Locate every blood parasite and identify its species.
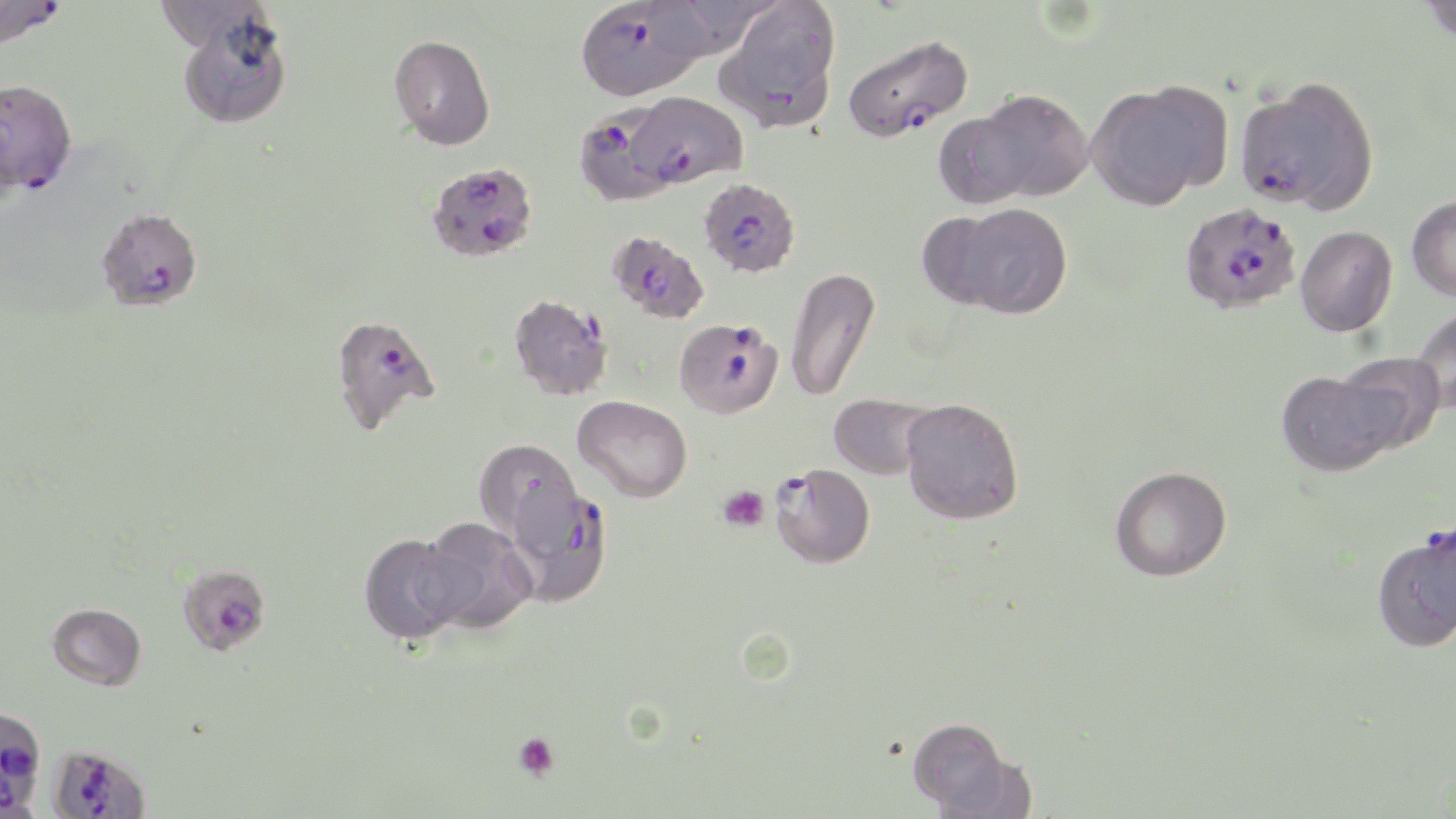
Approximate bounding boxes as (x1,y1)-(x2,y2) corner pairs in pixels.
Plasmodium falciparum-infected red blood cells: (0,0)-(67,50), (575,0)-(709,101), (841,33)-(973,143), (0,78)-(77,195), (1233,78)-(1378,213), (616,90)-(748,192), (579,105)-(690,208), (427,162)-(538,262), (699,177)-(801,278), (1179,202)-(1301,314), (95,207)-(203,312), (608,230)-(710,324), (507,293)-(614,401), (329,313)-(442,435), (674,317)-(784,419), (770,462)-(875,568), (504,482)-(614,607), (1406,530)-(1456,631), (176,563)-(272,656), (0,707)-(46,814), (48,744)-(151,819).
No Plasmodium ovale, Plasmodium malariae, Plasmodium vivax, Babesia divergens, or Trypanosoma brucei observed.

slide_level_diagnosis: Plasmodium falciparum
field_of_view: one of a larger specimen
modality: light microscopy
preparation: thin blood smear
platelet_locations: 'approximate bounding boxes as (x1,y1)-(x2,y2) corner pairs in pixels: (718,485)-(770,532), (512,730)-(560,781)'
magnification: 1000x
uninfected_red_blood_cell_locations: 'approximate bounding boxes as (x1,y1)-(x2,y2) corner pairs in pixels: (154,0)-(273,51), (1418,0)-(1456,45), (714,1)-(842,132), (175,8)-(294,130), (389,34)-(496,150), (1087,81)-(1230,209), (967,88)-(1095,203), (1407,195)-(1456,301), (936,201)-(1073,319), (1296,225)-(1397,337), (785,267)-(880,403), (1412,305)-(1456,414), (1334,352)-(1445,451), (1277,369)-(1404,476), (828,393)-(935,481), (573,395)-(692,502), (900,398)-(1024,525), (474,439)-(582,542), (1110,466)-(1232,581), (417,517)-(538,635), (359,533)-(468,645), (47,602)-(146,690), (907,717)-(1022,816)'
stain: May-Grünwald-Giemsa
image_size: 1456×819 pixels